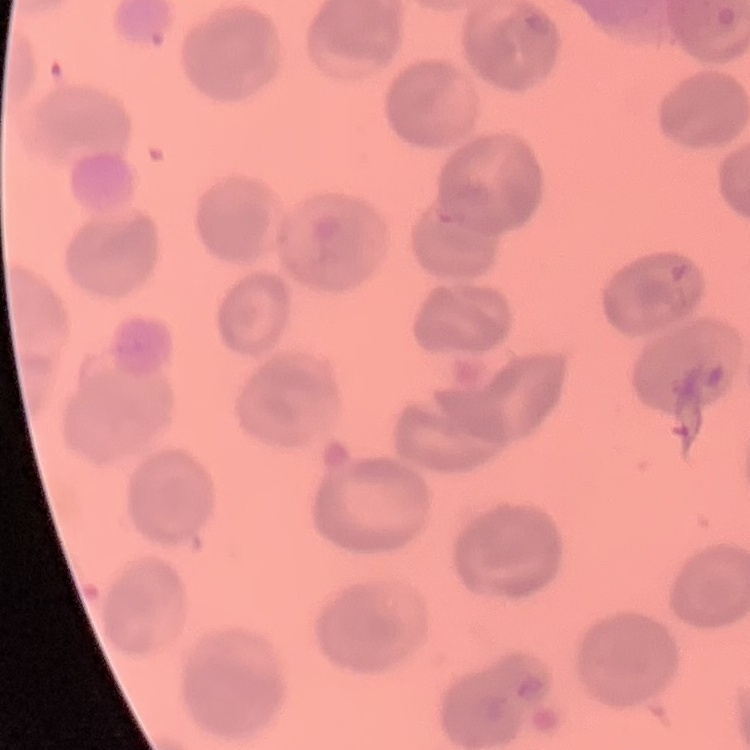
erythrocyte_morphology: no rouleaux formation
preparation: thin peripheral smear
image_type: square crop of a larger photomicrograph
stain: Field's or Giemsa